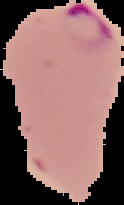
Cell region segmented out of the field of view; the surrounding area is masked to black. Image is 124×205 pixels. From a thin blood smear. Result: Plasmodium parasites detected.